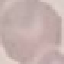 Result: negative for malaria parasites. Acquired by smartphone through the microscope eyepiece. Giemsa-stained preparation. Thin blood smear. Automatically extracted cell patch, resized to 64 × 64 pixels.